Comment on the morphology of the erythrocytes.
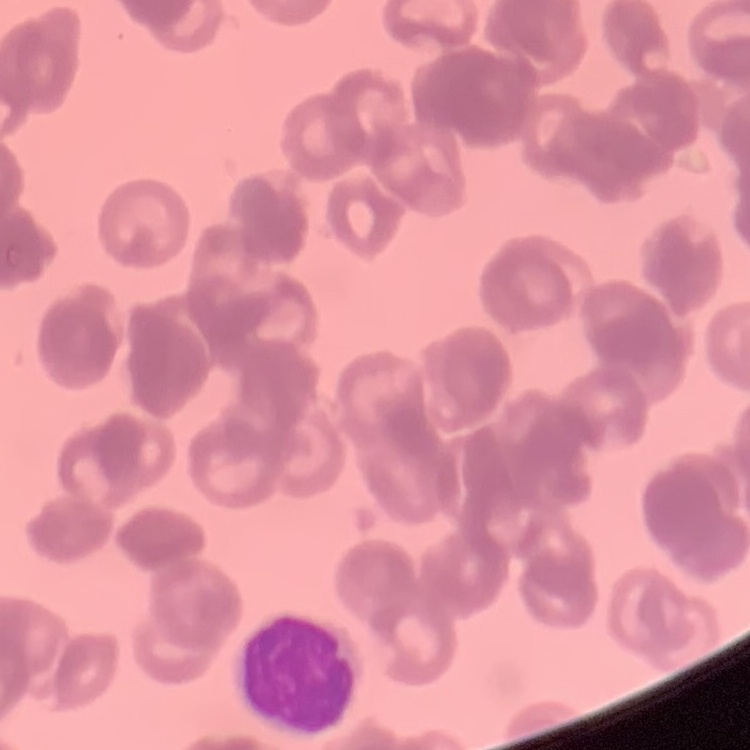

They show rouleaux formation.

stain = Field's or Giemsa
image type = one tile cut from a larger photomicrograph
preparation = thin blood film